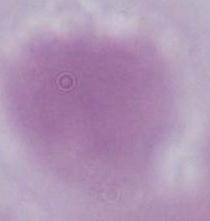

Summary:
  - Identification: red blood cell
  - Modality: photomicrograph
  - Magnification: 1000x